Locate every Plasmodium parasite.
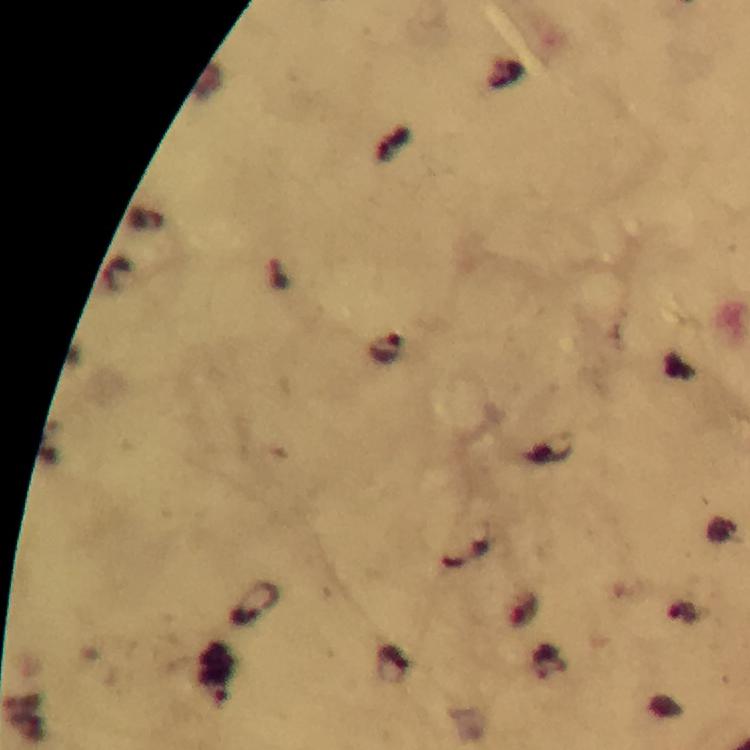
Approximate centers as [x, y] in pixels.
Plasmodium parasites: [387, 350], [254, 604], [682, 615], [545, 662], [394, 664].

Summary:
  - Immersion oil: applied
  - Cropped from: a single field of view
  - Preparation: thick smear
  - Stain: Giemsa
  - Image size: 750×750 pixels
  - Magnification: 100x
  - Capture: smartphone mounted on the microscope
  - Context: from a malaria diagnostic workup